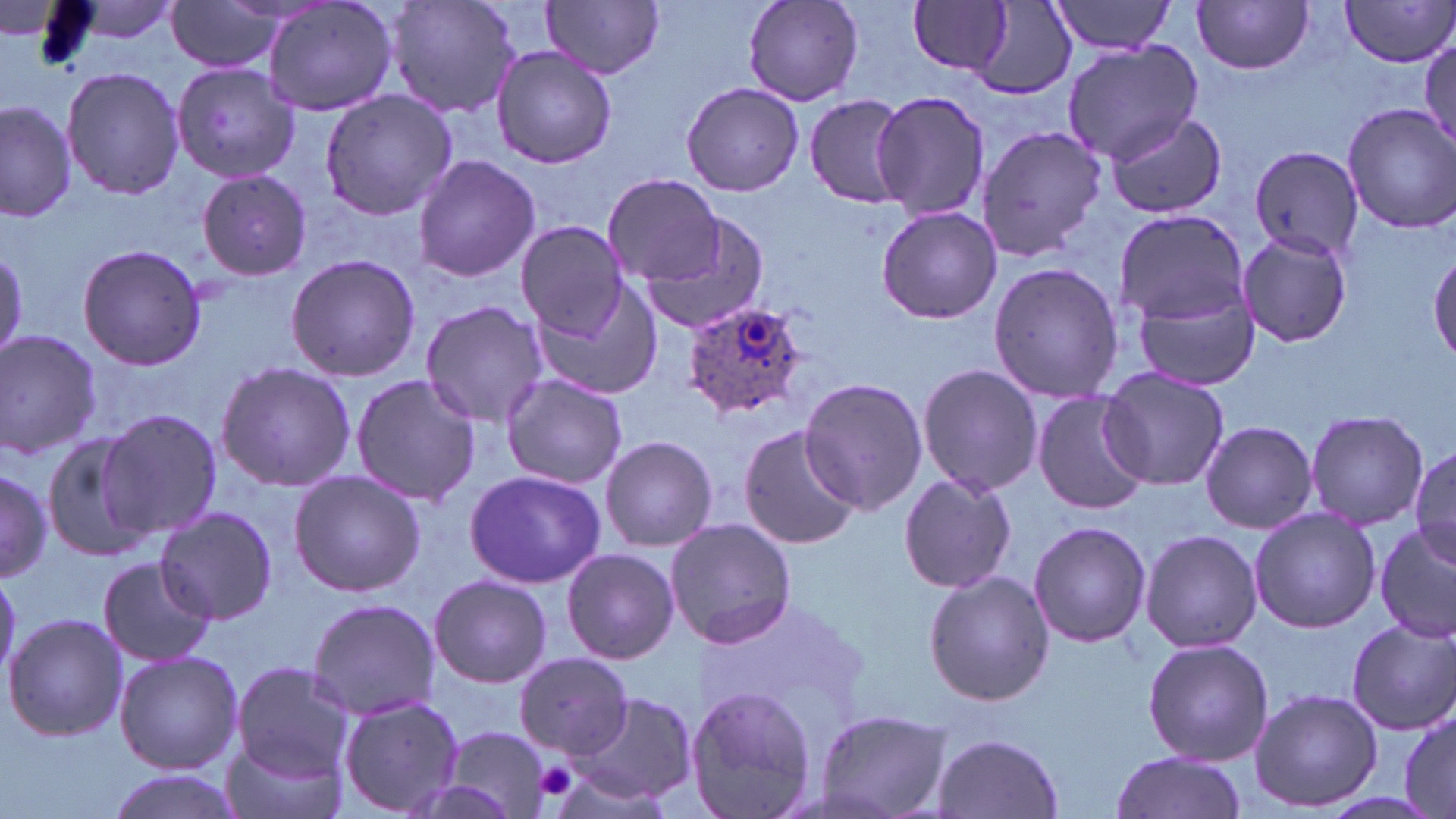

Approximate bounding boxes as (x1, y1, x2, y2) in pixels. Platelet locations: (535, 761, 580, 801). Uninfected red blood cell locations: (56, 0, 185, 49), (163, 0, 292, 75), (261, 0, 399, 117), (387, 0, 519, 119), (543, 0, 665, 78), (740, 0, 864, 108), (1339, 0, 1456, 68), (909, 1, 1013, 76), (1047, 1, 1178, 56), (1192, 1, 1316, 75), (954, 4, 1078, 97), (1060, 40, 1204, 164), (490, 43, 620, 170), (172, 62, 296, 188), (61, 66, 186, 201), (681, 82, 804, 196), (319, 89, 456, 219), (870, 90, 989, 222), (802, 95, 912, 207), (0, 100, 77, 224), (1341, 102, 1456, 233), (1106, 111, 1227, 219), (974, 123, 1107, 262), (1243, 143, 1364, 265), (412, 155, 541, 283), (194, 170, 312, 280), (604, 175, 726, 284), (875, 206, 1001, 323), (1113, 206, 1252, 340), (640, 213, 771, 335), (516, 221, 630, 337), (1234, 230, 1356, 348), (76, 243, 208, 372), (0, 249, 29, 358), (1430, 249, 1455, 366), (284, 253, 420, 383), (986, 262, 1124, 401), (1127, 268, 1262, 389), (528, 278, 665, 405), (420, 300, 550, 428), (0, 328, 104, 462), (215, 360, 354, 492), (917, 362, 1042, 497), (1099, 367, 1229, 491), (351, 374, 482, 506), (501, 376, 629, 490), (799, 379, 926, 514), (1032, 389, 1150, 514), (100, 407, 224, 542), (1306, 410, 1427, 532), (1200, 420, 1317, 533), (737, 423, 861, 549), (39, 429, 158, 564), (599, 434, 718, 552), (1408, 443, 1456, 565), (0, 463, 52, 584), (289, 467, 424, 597), (464, 468, 605, 590), (899, 471, 1018, 594), (154, 507, 280, 625), (1248, 508, 1382, 634), (665, 519, 798, 649), (1027, 521, 1152, 648), (1373, 522, 1456, 643), (1138, 529, 1263, 653), (561, 546, 680, 664), (97, 556, 215, 668), (924, 570, 1055, 705), (429, 574, 552, 688), (305, 596, 442, 720), (5, 610, 127, 742), (1346, 617, 1455, 735), (1142, 637, 1275, 765), (113, 649, 244, 775), (516, 650, 630, 757), (231, 662, 357, 782), (683, 685, 818, 819), (1248, 687, 1384, 812), (569, 689, 696, 804), (334, 694, 463, 817), (814, 707, 951, 819), (1397, 708, 1455, 818), (437, 727, 553, 817), (932, 733, 1064, 818), (218, 741, 343, 819), (1108, 750, 1243, 819), (102, 769, 242, 819). Plasmodium ovale-infected red blood cell locations: (681, 299, 811, 422). Slide-level diagnosis: Plasmodium ovale. Captured at 1000x magnification. May-Grünwald-Giemsa-stained preparation. Light microscopy. Image is 1456×819 pixels. One field of a larger specimen. Thin blood smear.